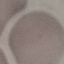

Malaria status: uninfected. Thin blood smear. Giemsa-stained preparation. Acquired by smartphone through the microscope eyepiece. Automatically extracted cell patch, resized to 64 × 64 pixels.